Point out each Plasmodium parasite.
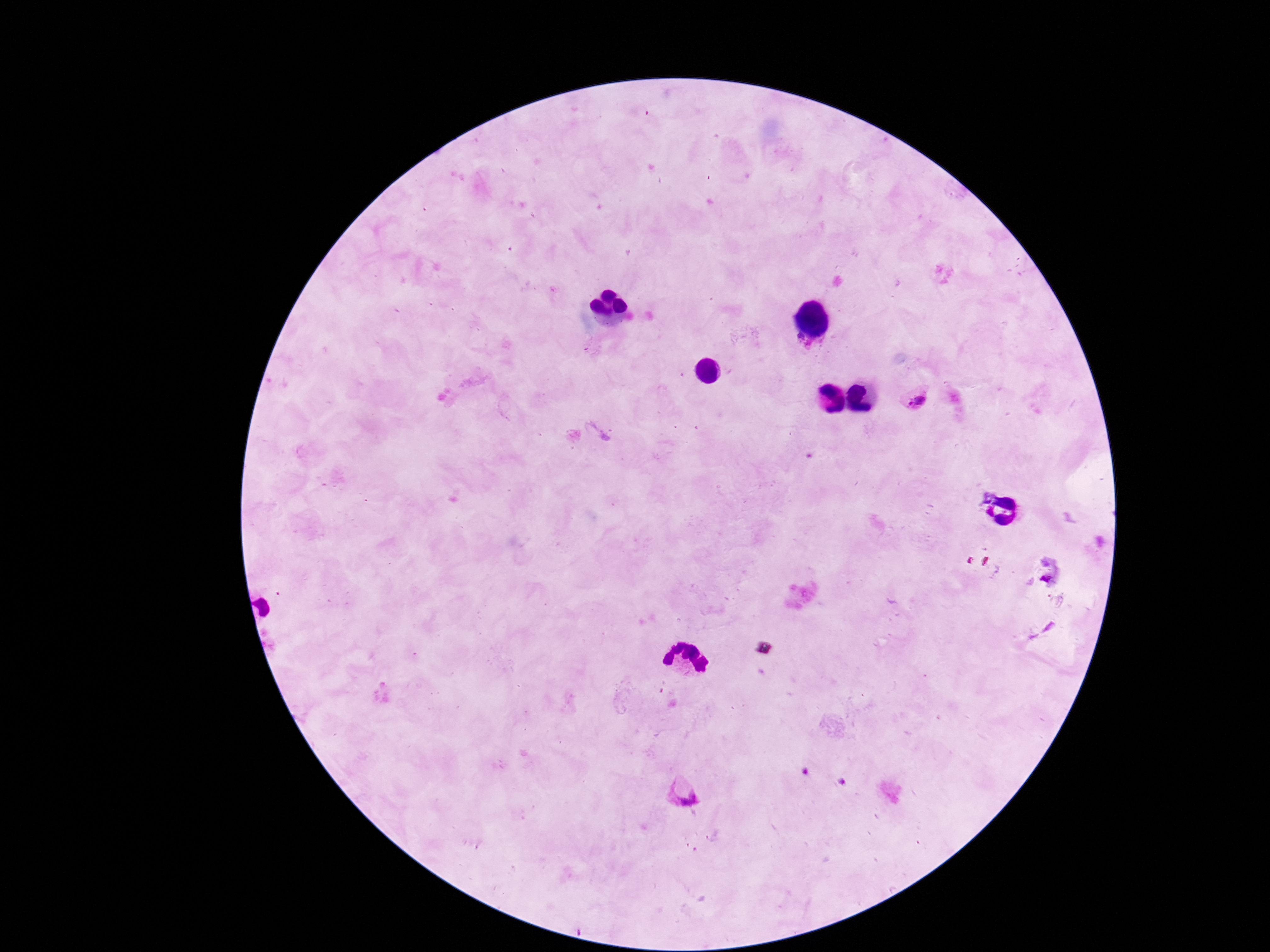

Approximate centers as [x, y] in pixels.
Plasmodium parasites: [918, 400], [684, 792].

field of view = single
magnification = 100x
preparation = thick blood smear
capture = smartphone camera through the microscope eyepiece
stain = Giemsa
image size = 1270×952 pixels
patient malaria status = positive